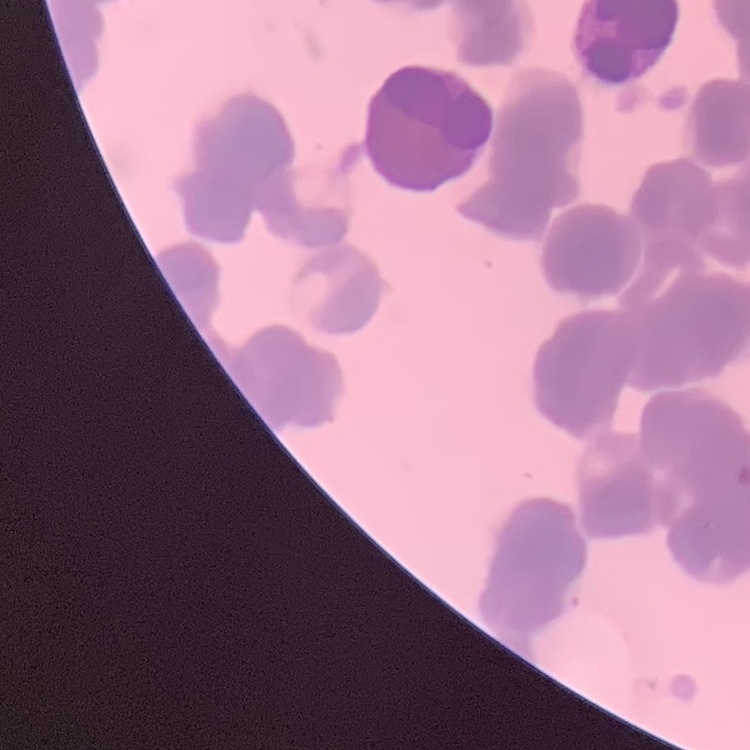

Summary:
  - Erythrocyte morphology: rouleaux formation
  - Preparation: thin blood smear
  - Stain: Field's or Giemsa
  - Image type: square crop of a larger photomicrograph